Outline Plasmodium malariae parasites and classify them by life-cycle stage.
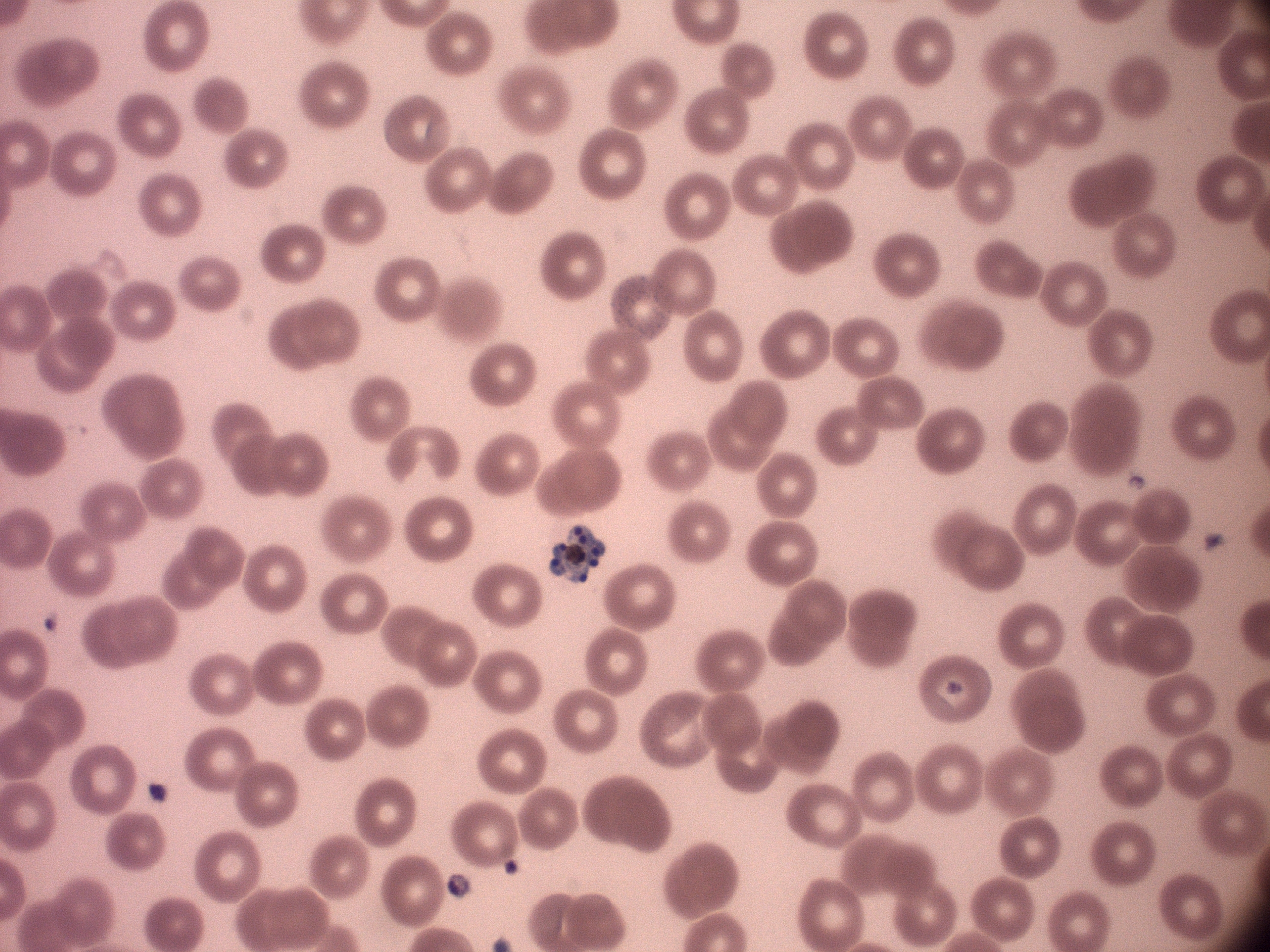

Approximate bounding boxes as named x1/y1/x2/y2 corners in pixels, from the source annotation, which is not necessarily exhaustive.
Schizonts: (x1=550, y1=523, x2=606, y2=583).

Species: Plasmodium malariae. One field from this slide. Giemsa-stained preparation. 100x magnification. Thin blood film. Image is 1270×952 pixels. Acquired with a Leica DM2000 optical microscope and its built-in camera.